Describe the morphology of the erythrocytes.
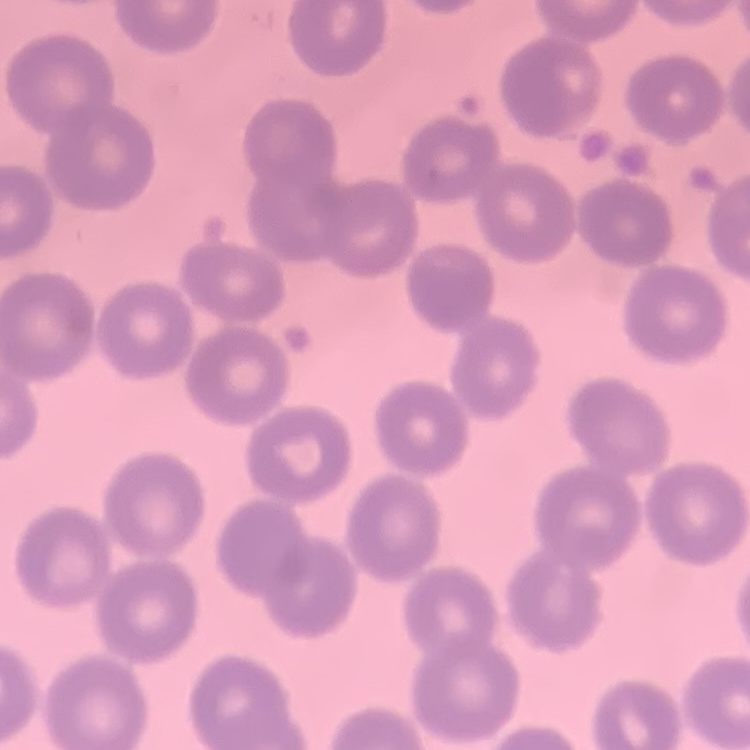
No rouleaux formation.

stain = Field's or Giemsa
preparation = thin blood smear
image type = one tile cut from a larger photomicrograph